State the blood parasite species.
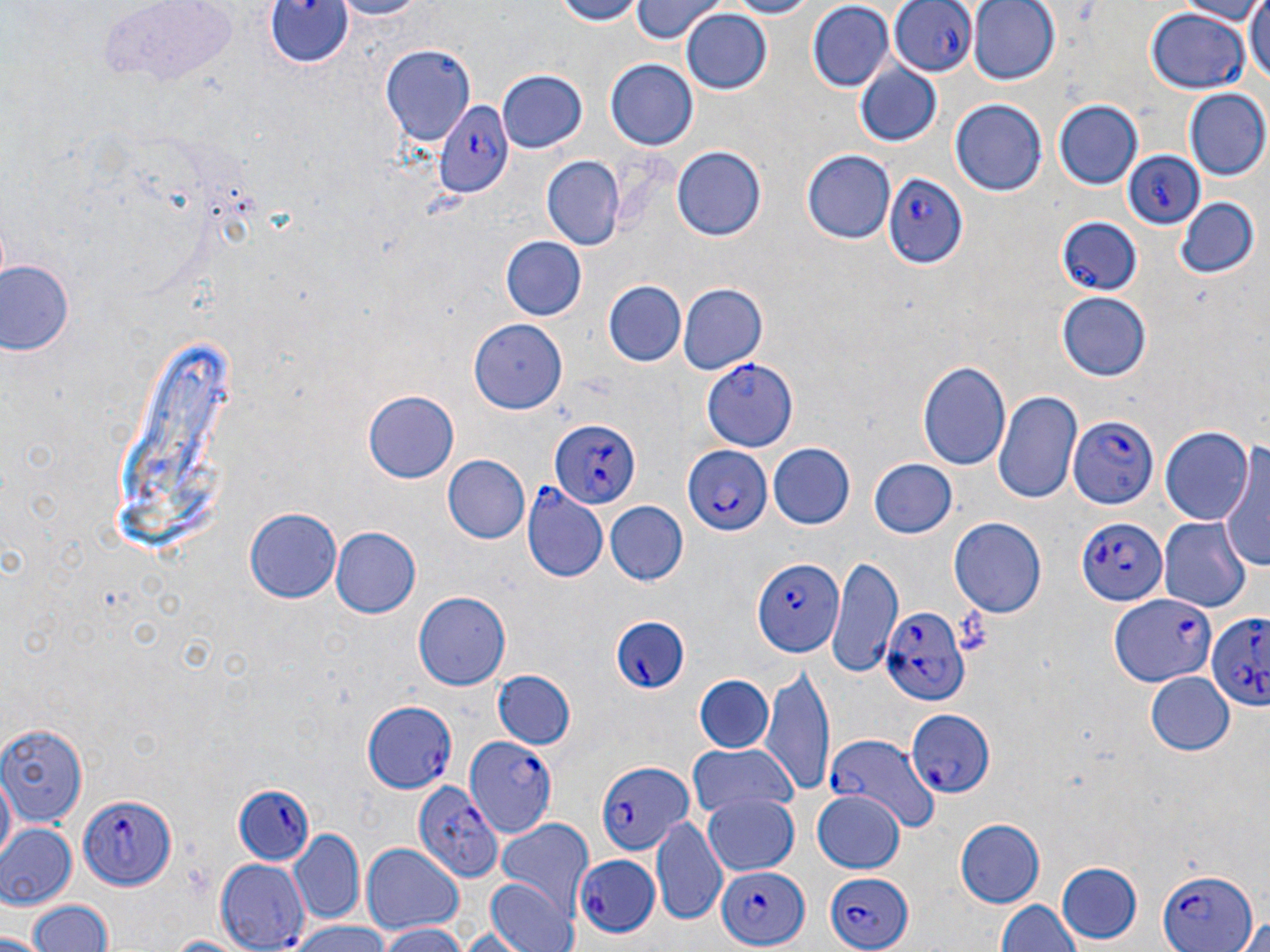
Plasmodium falciparum.

Approximate bounding boxes as named x1/y1/x2/y2 corners in pixels. Uninfected red blood cell locations: (x1=324, y1=0, x2=428, y2=19), (x1=540, y1=0, x2=653, y2=25), (x1=628, y1=0, x2=727, y2=42), (x1=720, y1=0, x2=822, y2=18), (x1=965, y1=0, x2=1061, y2=86), (x1=1170, y1=0, x2=1267, y2=22), (x1=1245, y1=0, x2=1270, y2=88), (x1=806, y1=1, x2=892, y2=89), (x1=679, y1=10, x2=772, y2=95), (x1=381, y1=43, x2=476, y2=149), (x1=607, y1=59, x2=699, y2=151), (x1=852, y1=62, x2=943, y2=147), (x1=497, y1=70, x2=588, y2=153), (x1=1186, y1=90, x2=1268, y2=179), (x1=952, y1=97, x2=1047, y2=196), (x1=1054, y1=100, x2=1142, y2=190), (x1=672, y1=146, x2=768, y2=242), (x1=802, y1=151, x2=896, y2=244), (x1=540, y1=156, x2=625, y2=251), (x1=1172, y1=195, x2=1258, y2=280), (x1=500, y1=237, x2=588, y2=321), (x1=0, y1=258, x2=75, y2=358), (x1=604, y1=282, x2=685, y2=366), (x1=676, y1=282, x2=769, y2=377), (x1=1055, y1=291, x2=1152, y2=382), (x1=467, y1=320, x2=566, y2=414), (x1=919, y1=358, x2=1009, y2=471), (x1=933, y1=374, x2=1079, y2=483), (x1=996, y1=389, x2=1080, y2=504), (x1=363, y1=390, x2=461, y2=482), (x1=1158, y1=424, x2=1254, y2=526), (x1=769, y1=443, x2=855, y2=529), (x1=1220, y1=443, x2=1268, y2=577), (x1=441, y1=455, x2=529, y2=544), (x1=867, y1=457, x2=958, y2=539), (x1=605, y1=502, x2=687, y2=585), (x1=245, y1=505, x2=340, y2=601), (x1=950, y1=517, x2=1044, y2=618), (x1=1159, y1=517, x2=1251, y2=612), (x1=330, y1=526, x2=421, y2=617), (x1=828, y1=557, x2=901, y2=676), (x1=414, y1=592, x2=510, y2=689), (x1=761, y1=666, x2=835, y2=797), (x1=491, y1=670, x2=577, y2=751), (x1=1144, y1=672, x2=1232, y2=756), (x1=695, y1=675, x2=775, y2=754), (x1=0, y1=720, x2=86, y2=826), (x1=686, y1=743, x2=796, y2=822), (x1=2, y1=772, x2=17, y2=867), (x1=809, y1=789, x2=906, y2=875), (x1=702, y1=792, x2=800, y2=876), (x1=652, y1=816, x2=729, y2=926), (x1=498, y1=818, x2=595, y2=921), (x1=955, y1=818, x2=1044, y2=908), (x1=0, y1=825, x2=77, y2=910), (x1=286, y1=831, x2=365, y2=926), (x1=358, y1=841, x2=467, y2=936), (x1=212, y1=859, x2=308, y2=951), (x1=1057, y1=862, x2=1143, y2=945), (x1=487, y1=877, x2=579, y2=952), (x1=26, y1=899, x2=116, y2=952), (x1=994, y1=901, x2=1080, y2=952), (x1=1236, y1=914, x2=1270, y2=952), (x1=287, y1=923, x2=396, y2=952), (x1=373, y1=924, x2=471, y2=952), (x1=0, y1=932, x2=47, y2=952), (x1=161, y1=932, x2=254, y2=952). Plasmodium falciparum-infected red blood cell locations: (x1=264, y1=1, x2=352, y2=71), (x1=892, y1=1, x2=974, y2=78), (x1=1148, y1=6, x2=1249, y2=93), (x1=432, y1=97, x2=513, y2=201), (x1=1124, y1=151, x2=1208, y2=231), (x1=884, y1=174, x2=969, y2=267), (x1=1055, y1=216, x2=1139, y2=295), (x1=702, y1=358, x2=798, y2=451), (x1=1069, y1=413, x2=1159, y2=511), (x1=548, y1=418, x2=641, y2=511), (x1=682, y1=444, x2=769, y2=534), (x1=522, y1=485, x2=608, y2=585), (x1=1075, y1=515, x2=1167, y2=605), (x1=751, y1=559, x2=844, y2=660), (x1=1111, y1=592, x2=1218, y2=685), (x1=882, y1=606, x2=969, y2=708), (x1=1207, y1=611, x2=1270, y2=718), (x1=606, y1=616, x2=689, y2=694), (x1=361, y1=699, x2=459, y2=794), (x1=906, y1=709, x2=996, y2=798), (x1=462, y1=731, x2=559, y2=841), (x1=825, y1=736, x2=938, y2=833), (x1=596, y1=757, x2=691, y2=857), (x1=414, y1=781, x2=502, y2=883), (x1=235, y1=784, x2=317, y2=866), (x1=79, y1=793, x2=177, y2=891), (x1=572, y1=852, x2=663, y2=939), (x1=714, y1=859, x2=817, y2=951), (x1=1156, y1=867, x2=1261, y2=952), (x1=822, y1=873, x2=911, y2=947). Light microscopy. Thin blood film. May-Grünwald-Giemsa stain. Image is 1270×952 pixels. One field of a larger specimen. Captured at 1000x magnification.